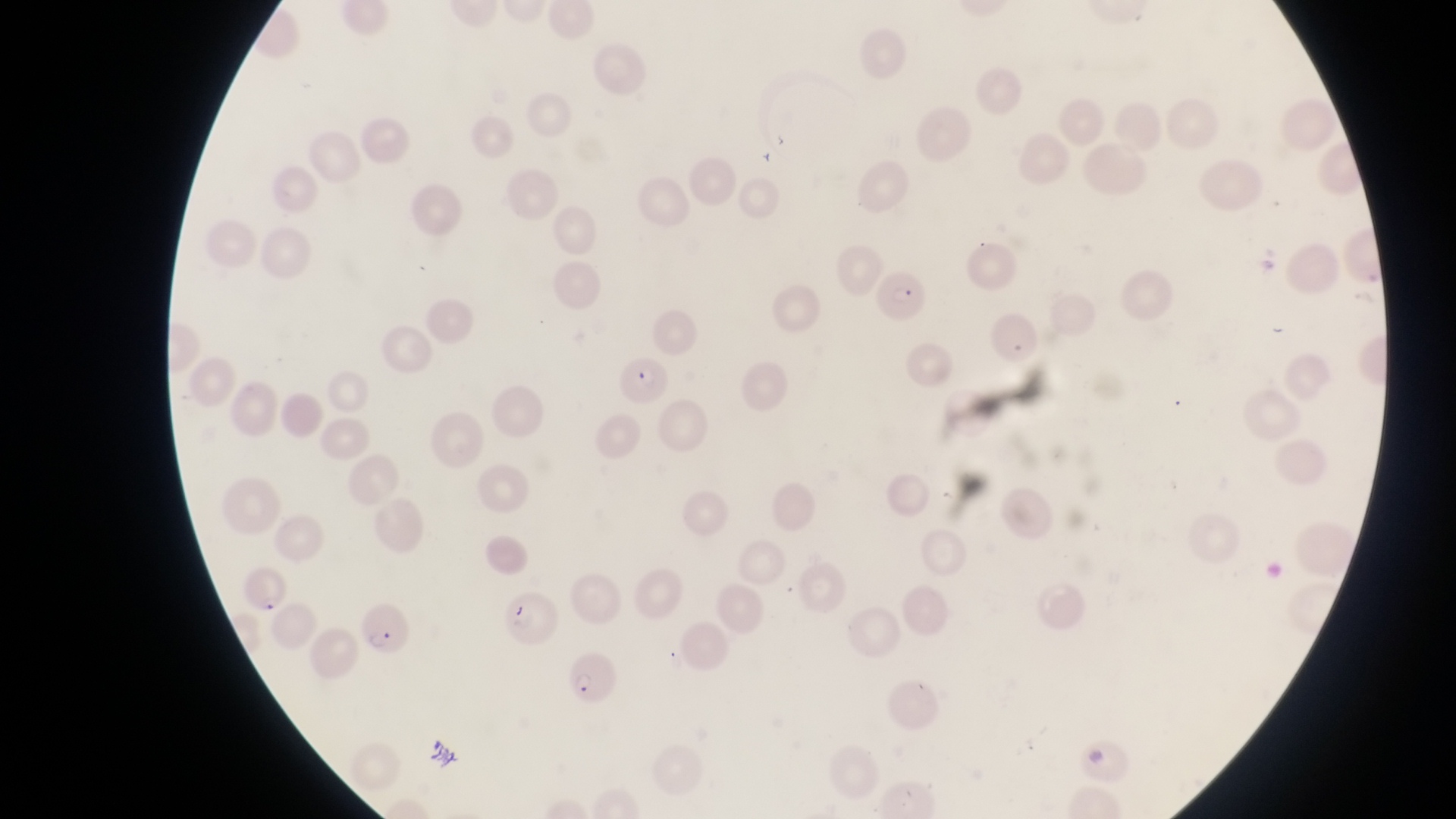

Approximate bounding boxes as (left, top, right, bottom) in pixels.
Summary:
  - Parasitised red blood cell locations: (872, 268, 936, 331), (620, 356, 673, 403), (234, 563, 289, 615), (360, 602, 405, 655), (570, 654, 623, 711)
  - Capture: smartphone photograph through the eyepiece of an Olympus CX-23 microscope
  - Preparation: thin blood smear
  - Country: Uganda
  - Field of view: single
  - Image size: 1456×819 pixels
  - Magnification: 1000x